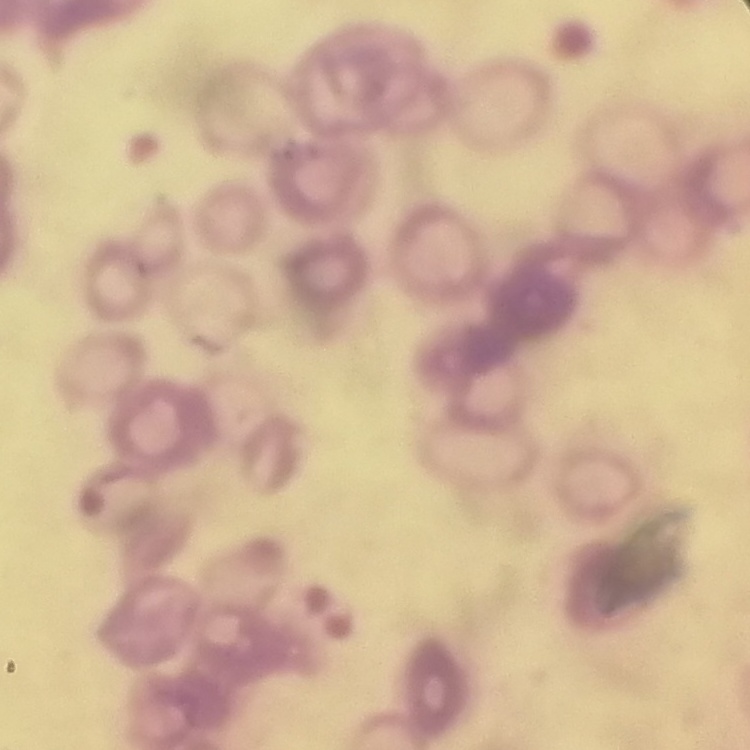

The red blood cells show rouleaux formation. One tile cut from a larger photomicrograph. Thin blood smear. Stained with either Field's or Giemsa.